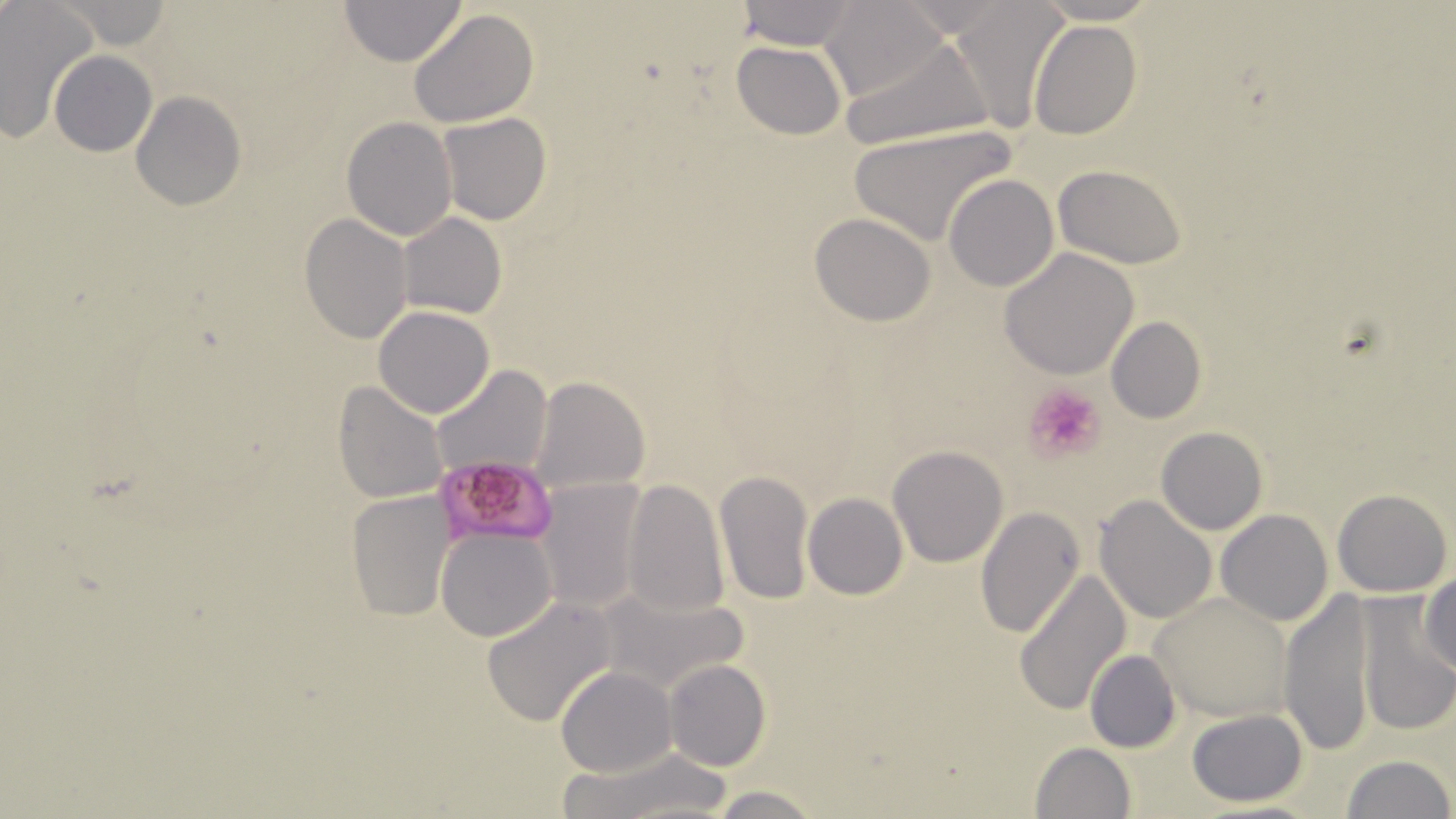

{
  "slide_level_diagnosis": "Plasmodium falciparum",
  "platelet_locations": "approximate bounding boxes as [x1, y1, x2, y2] in pixels: [1025, 383, 1106, 460]",
  "plasmodium_falciparum_infected_red_blood_cell_locations": "approximate bounding boxes as [x1, y1, x2, y2] in pixels: [437, 456, 560, 546]",
  "field_of_view": "one of a larger specimen",
  "uninfected_red_blood_cell_locations": "approximate bounding boxes as [x1, y1, x2, y2] in pixels: [339, 0, 466, 66], [738, 0, 858, 48], [1030, 0, 1162, 24], [820, 1, 944, 102], [0, 2, 99, 143], [58, 2, 173, 49], [945, 3, 1067, 128], [408, 8, 540, 129], [1029, 18, 1142, 139], [840, 37, 996, 150], [731, 41, 846, 140], [50, 51, 158, 156], [131, 92, 246, 210], [438, 112, 551, 225], [341, 116, 457, 241], [846, 125, 1016, 246], [1053, 164, 1186, 267], [944, 173, 1059, 291], [299, 212, 413, 344], [809, 212, 937, 326], [397, 213, 507, 318], [999, 248, 1139, 379], [374, 306, 493, 418], [1105, 315, 1206, 425], [431, 365, 553, 481], [530, 376, 650, 494], [333, 381, 449, 503], [1155, 426, 1268, 535], [887, 445, 1010, 567], [713, 468, 815, 607], [534, 478, 648, 614], [622, 478, 730, 618], [1333, 489, 1452, 595], [347, 491, 457, 622], [803, 493, 909, 600], [1094, 495, 1216, 624], [974, 506, 1085, 639], [1216, 509, 1332, 626], [437, 528, 556, 642], [1015, 569, 1131, 716], [1420, 574, 1456, 675], [1278, 586, 1376, 758], [594, 588, 751, 699], [1150, 592, 1294, 720], [1353, 595, 1454, 737], [481, 596, 619, 728], [1085, 649, 1181, 752], [663, 660, 770, 772], [555, 666, 676, 777], [1185, 709, 1310, 806], [1029, 742, 1136, 819], [564, 750, 733, 816], [1341, 753, 1453, 819], [710, 785, 821, 819]",
  "magnification": "1000x",
  "preparation": "thin blood smear",
  "modality": "optical microscopy",
  "image_size": "1456×819 pixels",
  "stain": "May-Grünwald-Giemsa"
}